Name the blood parasite species.
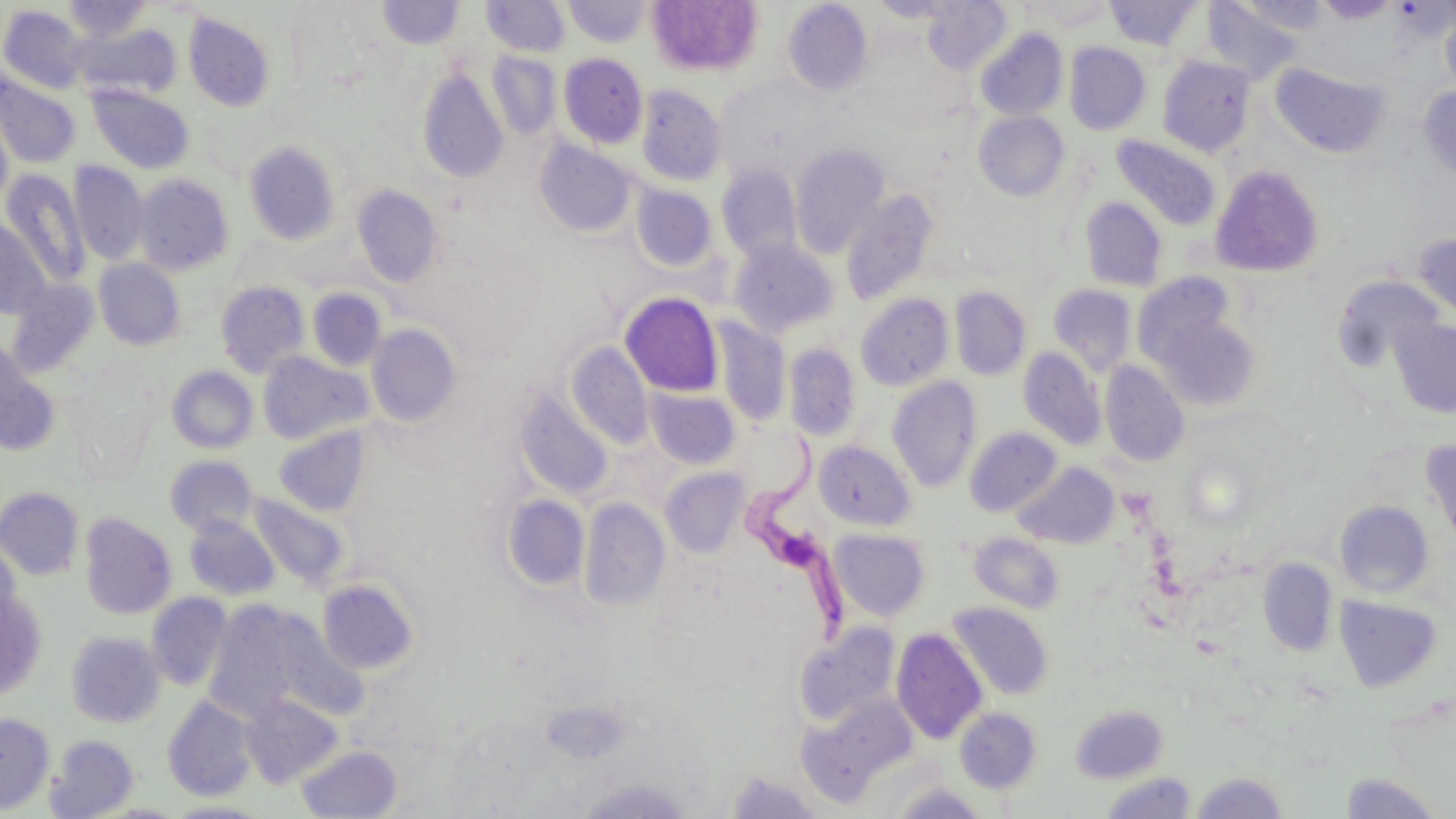

Trypanosoma brucei.

Summary:
  - Coordinate format: approximate bounding boxes as (x1, y1, x2, y2) in pixels
  - Uninfected red blood cell locations: (62, 0, 153, 41), (482, 0, 570, 56), (646, 0, 762, 76), (868, 0, 962, 22), (923, 0, 1012, 74), (1201, 0, 1301, 84), (1315, 0, 1398, 23), (377, 1, 464, 49), (564, 1, 650, 47), (1024, 1, 1115, 30), (1105, 1, 1202, 51), (1237, 1, 1328, 35), (784, 2, 872, 95), (1, 4, 89, 94), (1440, 6, 1456, 98), (183, 12, 276, 111), (74, 23, 180, 99), (975, 28, 1068, 121), (1064, 42, 1151, 135), (487, 51, 561, 141), (558, 54, 647, 148), (1157, 56, 1256, 156), (1270, 62, 1390, 158), (417, 67, 509, 183), (0, 74, 81, 169), (88, 85, 193, 173), (636, 85, 727, 187), (1419, 86, 1456, 184), (0, 107, 14, 217), (973, 111, 1069, 201), (1111, 134, 1222, 231), (535, 138, 638, 238), (244, 140, 341, 245), (790, 142, 890, 259), (69, 162, 149, 266), (716, 163, 803, 263), (1210, 165, 1325, 278), (1, 170, 90, 287), (133, 174, 234, 274), (630, 183, 717, 271), (352, 185, 442, 286), (841, 188, 939, 305), (1080, 196, 1168, 291), (0, 218, 52, 321), (1412, 231, 1456, 319), (729, 240, 838, 337), (93, 259, 186, 350), (1132, 272, 1238, 371), (1330, 273, 1445, 374), (6, 279, 100, 378), (215, 281, 310, 378), (1048, 284, 1137, 374), (950, 286, 1031, 381), (307, 288, 386, 371), (620, 292, 724, 397), (855, 293, 953, 391), (1149, 307, 1263, 412), (713, 318, 792, 425), (1390, 318, 1456, 418), (365, 326, 460, 427), (0, 340, 60, 454), (566, 342, 653, 449), (783, 342, 861, 441), (1019, 347, 1106, 450), (257, 352, 372, 445), (1100, 361, 1190, 467), (166, 366, 258, 454), (887, 376, 981, 492), (646, 388, 740, 469), (514, 389, 613, 500), (274, 426, 370, 516), (965, 427, 1062, 517), (1421, 439, 1456, 549), (814, 440, 914, 530), (164, 455, 259, 536), (1013, 462, 1119, 549), (659, 467, 749, 558), (0, 487, 84, 581), (247, 493, 351, 590), (501, 495, 589, 591), (579, 498, 670, 611), (1334, 500, 1434, 598), (79, 512, 176, 619), (184, 515, 279, 601), (828, 528, 931, 621), (968, 532, 1064, 614), (0, 538, 23, 634), (1257, 556, 1338, 657), (317, 578, 419, 676), (1, 591, 48, 699), (146, 592, 233, 692), (1334, 595, 1443, 693), (203, 601, 342, 723), (947, 601, 1053, 700), (266, 618, 367, 721), (793, 622, 901, 727), (891, 627, 988, 744), (66, 631, 165, 727), (241, 695, 342, 787), (162, 696, 259, 802), (801, 697, 918, 803), (1072, 703, 1169, 784), (955, 707, 1042, 793), (0, 712, 54, 813), (47, 734, 139, 817), (296, 744, 402, 818), (726, 770, 825, 818), (1189, 771, 1291, 818), (1100, 772, 1197, 818), (1339, 772, 1443, 818), (165, 801, 271, 818)
  - Trypanosoma brucei locations: (739, 431, 870, 643)
  - Image size: 1456×819 pixels
  - Stain: May-Grünwald-Giemsa
  - Magnification: 1000x
  - Preparation: thin blood film
  - Field of view: single
  - Modality: light microscopy